Classify this cell by malaria status.
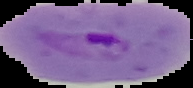

Parasitized.

{
  "preparation": "thin blood film",
  "image_size": "193×88 pixels",
  "image_type": "cell region segmented out of the field of view; surrounding area masked to black"
}